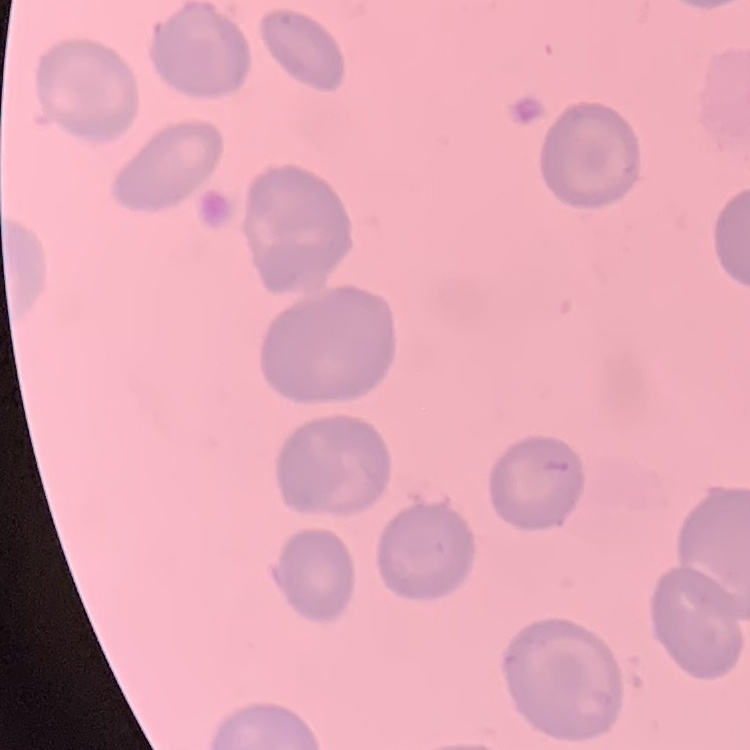
The red blood cells exhibit no rouleaux formation. One tile cut from a larger photomicrograph. Thin blood smear. Field's or Giemsa stain.